Comment on the morphology of the red blood cells.
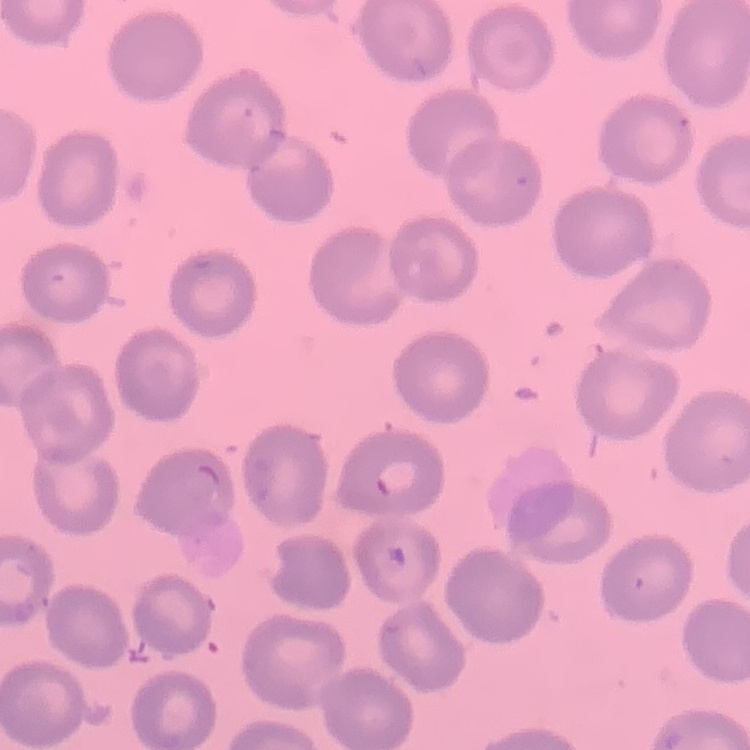
They show no rouleaux formation.

Summary:
  - Stain: Field's or Giemsa
  - Preparation: thin peripheral smear
  - Image type: square crop of a larger photomicrograph